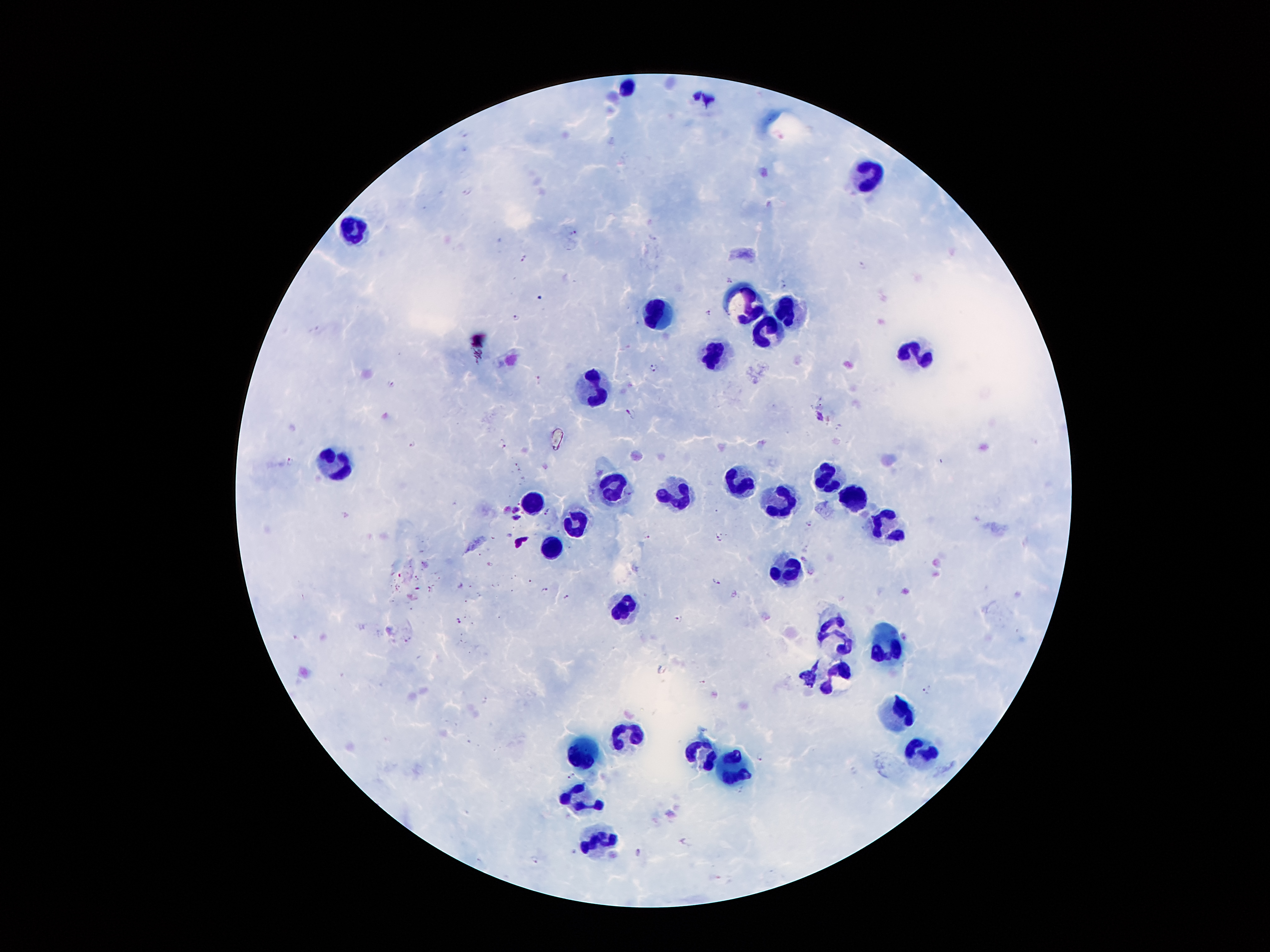
Approximate centers as (x, y) in pixels.
Summary:
  - Plasmodium parasite locations: (467, 190), (575, 233), (524, 259), (863, 265), (729, 279), (783, 284), (709, 313), (516, 316), (655, 366), (538, 380), (631, 413), (412, 444), (502, 444), (291, 460), (517, 467), (546, 511), (809, 523), (646, 535), (719, 537), (716, 580), (462, 585), (543, 588), (566, 596), (679, 618), (459, 620), (408, 638), (701, 682), (926, 691), (760, 756), (572, 776), (637, 853), (534, 859)
  - Leukocyte locations: (626, 88), (869, 174), (355, 233), (748, 302), (786, 309), (658, 312), (769, 334), (707, 355), (921, 357), (594, 387), (335, 458), (827, 480), (738, 483), (618, 488), (854, 496), (529, 498), (679, 500), (784, 501), (888, 525), (578, 526), (548, 545), (790, 569), (623, 607), (837, 634), (890, 648), (832, 676), (901, 711), (623, 735), (918, 750), (703, 751), (579, 755), (735, 769), (582, 796), (597, 838)
  - Capture: smartphone through the microscope eyepiece
  - Magnification: 100x
  - Image size: 1270×952 pixels
  - Stain: Giemsa
  - Preparation: thick blood smear
  - Patient malaria status: infected with Plasmodium falciparum
  - Field of view: single